Assess the morphology of the red blood cells.
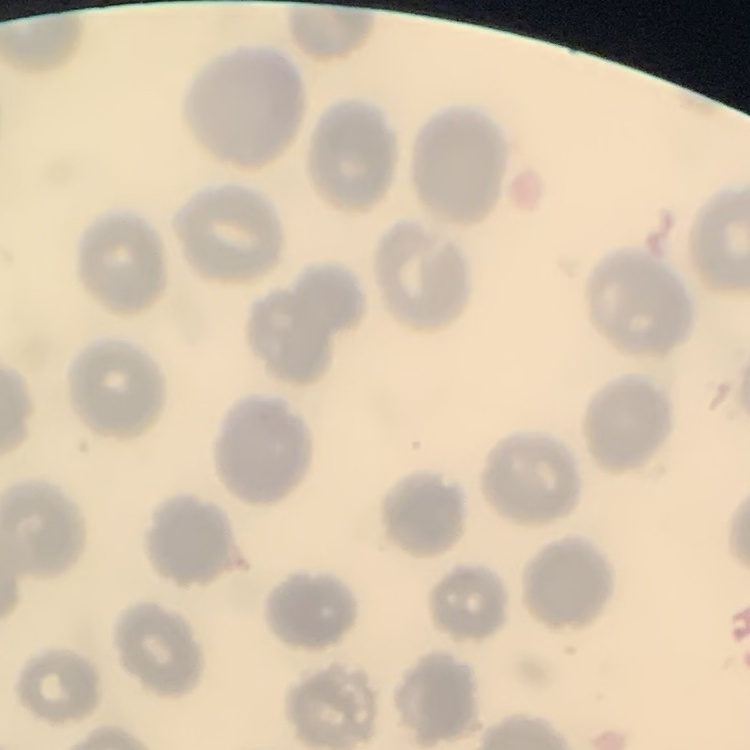
No rouleaux formation.

Square crop of a larger photomicrograph. Thin blood film. Stained with either Field's or Giemsa.